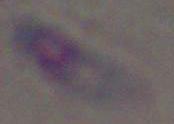

identification = Toxoplasma gondii
magnification = 1000x
modality = photomicrograph